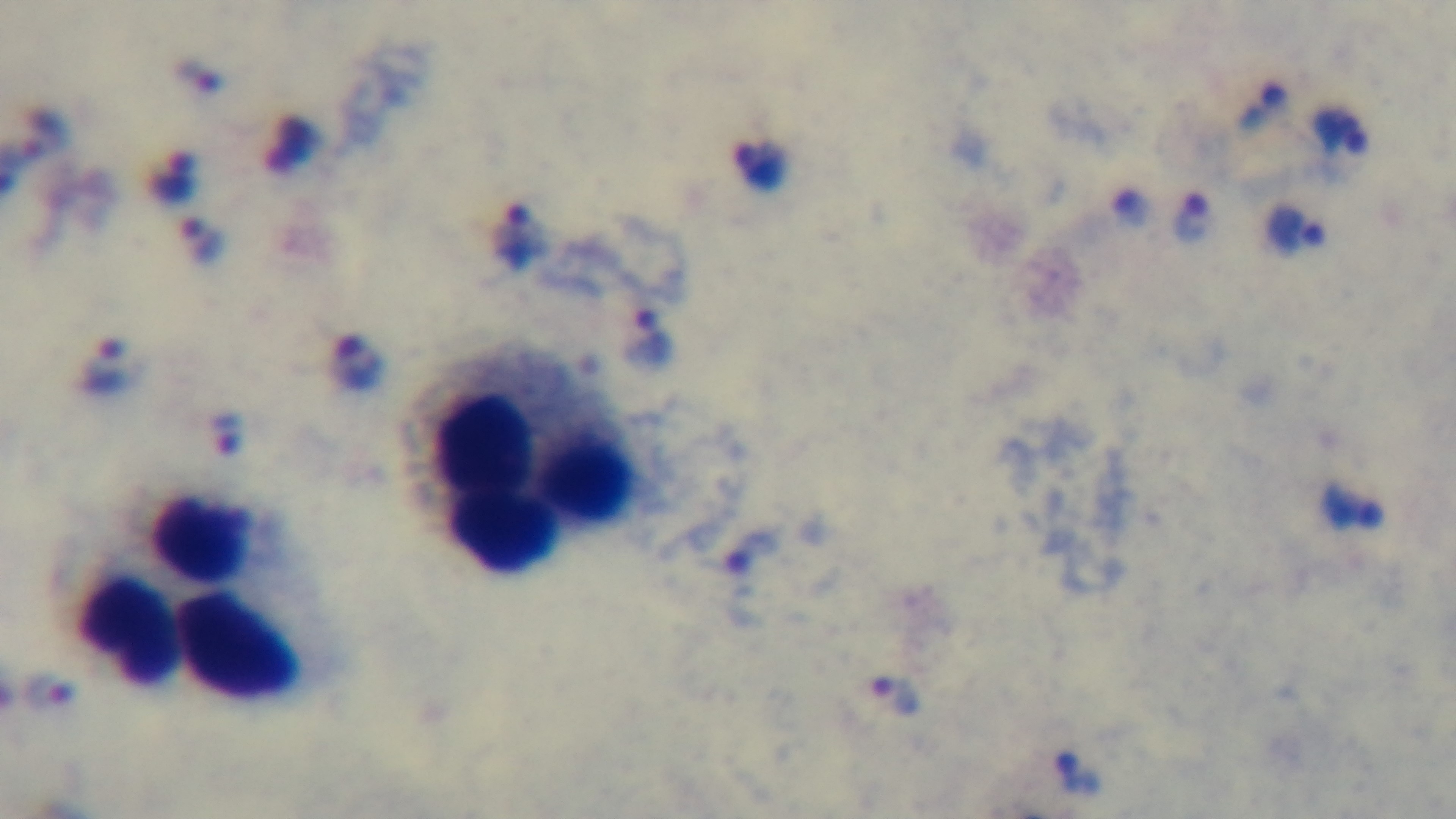

{
  "field_of_view": "one from the slide",
  "objective": "100x oil immersion",
  "stain": "Giemsa",
  "modality": "light microscopy",
  "capture": "mounted 4K digital camera",
  "malaria_status": "infected",
  "preparation": "thick blood film"
}